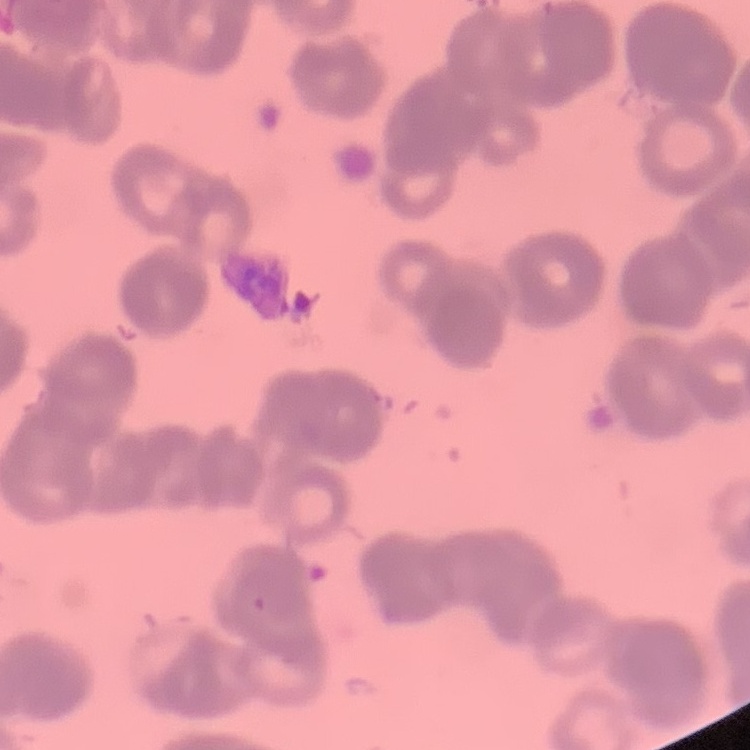
erythrocyte morphology = rouleaux formation
image type = one tile cut from a larger photomicrograph
stain = Field's or Giemsa
preparation = thin blood smear